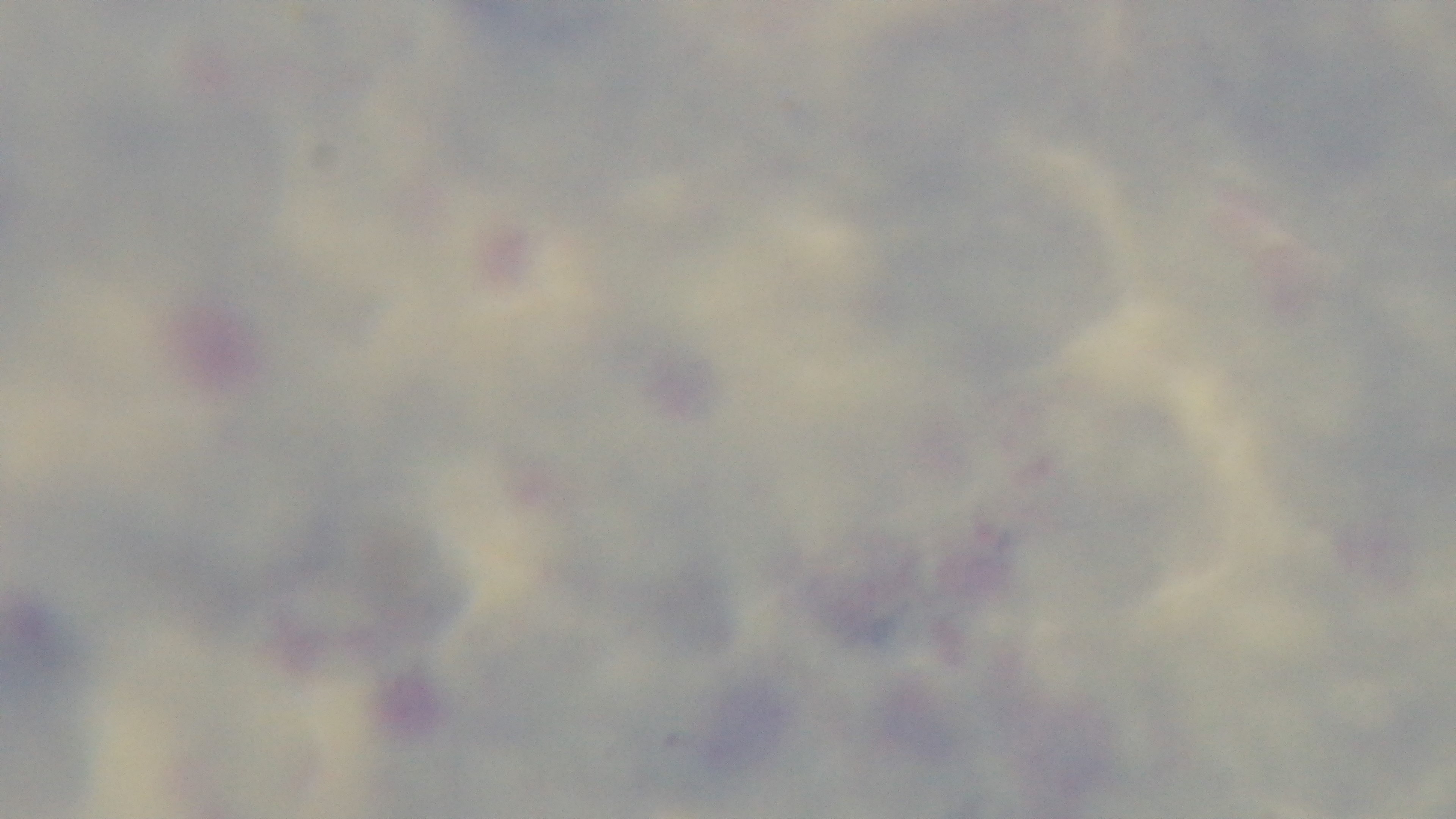

Summary:
  - Capture: mounted 4K digital camera
  - Stain: Giemsa
  - Field of view: single
  - Objective: 100x oil immersion
  - Preparation: thick
  - Modality: light microscopy
  - Malaria status: uninfected